Give the extent of all Plasmodium falciparum-infected red blood cells.
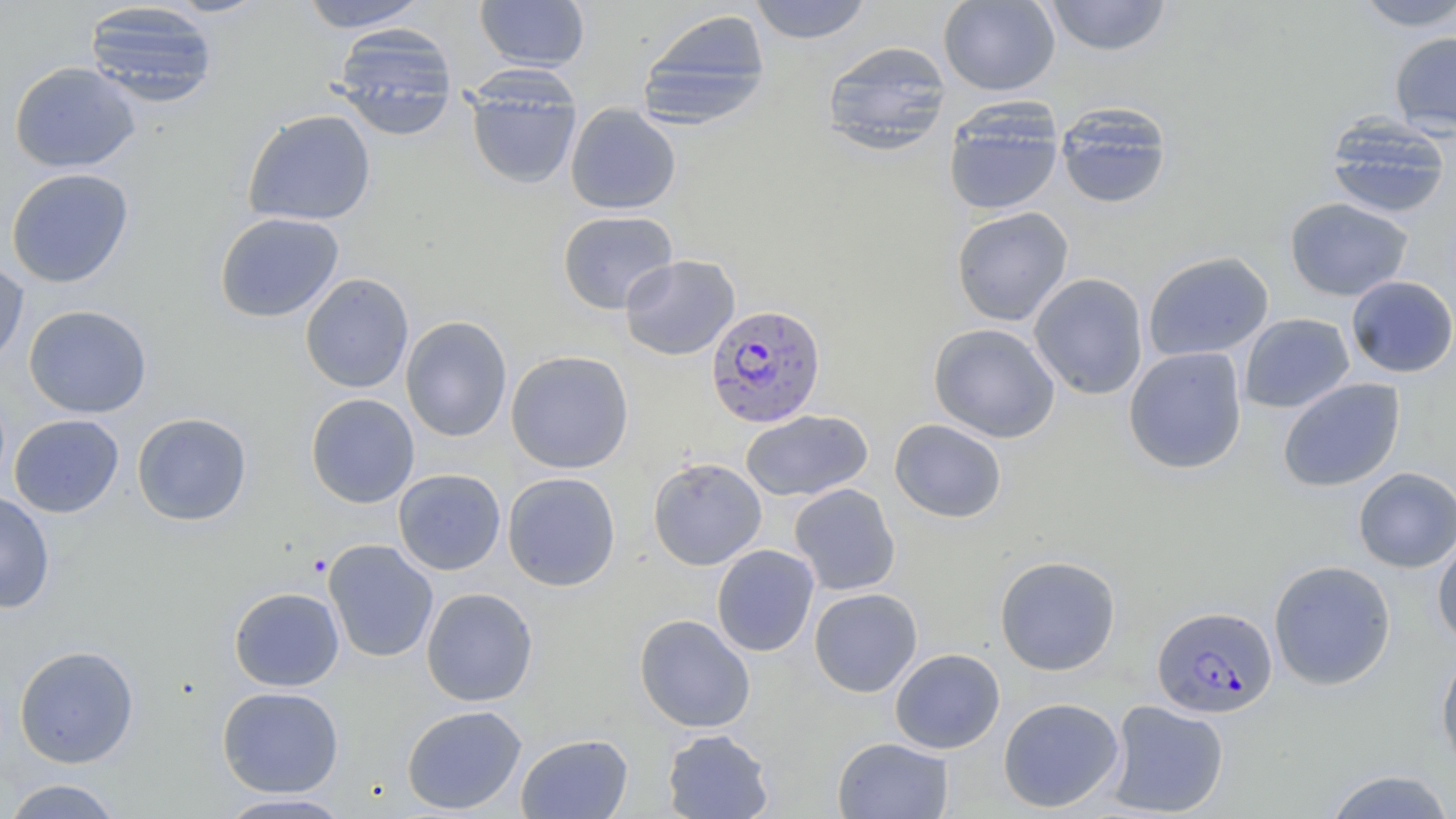

Approximate bounding boxes as (x1,y1)-(x2,y2) corner pairs in pixels.
Plasmodium falciparum-infected red blood cells: (705,303)-(826,428), (1151,605)-(1277,719).

Uninfected red blood cell locations: (162,0)-(271,17), (297,0)-(431,32), (475,0)-(590,71), (749,0)-(873,44), (938,0)-(1060,96), (1044,0)-(1172,56), (1351,0)-(1456,31), (84,2)-(219,107), (637,9)-(771,127), (332,24)-(458,141), (1389,31)-(1456,135), (822,40)-(952,154), (9,61)-(141,173), (465,76)-(582,190), (565,103)-(681,215), (1056,103)-(1172,209), (944,104)-(1063,216), (242,109)-(376,227), (1325,116)-(1452,219), (6,168)-(134,287), (1285,197)-(1413,301), (952,206)-(1073,326), (558,210)-(678,314), (214,212)-(344,323), (1143,251)-(1274,361), (619,254)-(740,360), (0,256)-(29,369), (300,273)-(414,393), (1028,273)-(1149,400), (1345,275)-(1456,378), (24,304)-(152,418), (1239,313)-(1355,413), (401,315)-(512,442), (928,323)-(1061,443), (1124,346)-(1247,474), (506,350)-(634,473), (1278,378)-(1405,492), (305,393)-(419,508), (740,410)-(873,502), (132,412)-(252,526), (9,414)-(124,518), (889,418)-(1007,523), (648,457)-(767,570), (1353,467)-(1456,572), (393,469)-(506,575), (502,471)-(621,591), (789,483)-(901,596), (0,490)-(55,613), (1432,531)-(1456,649), (323,539)-(438,662), (711,544)-(819,657), (994,555)-(1121,676), (1268,559)-(1396,690), (229,587)-(344,691), (421,587)-(538,707), (809,588)-(923,697), (633,614)-(756,732), (14,645)-(139,768), (889,648)-(1005,754), (1436,648)-(1456,774), (217,685)-(344,797), (998,697)-(1124,813), (1105,700)-(1229,817), (401,704)-(527,815), (661,728)-(775,818), (515,733)-(633,818), (832,736)-(954,818), (1322,769)-(1456,818), (1,778)-(125,818), (215,793)-(356,818). Slide-level diagnosis: Plasmodium falciparum. Image is 1456×819 pixels. Optical microscopy. Thin blood smear. Captured at 1000x magnification. Single field of view. May-Grünwald-Giemsa-stained preparation.